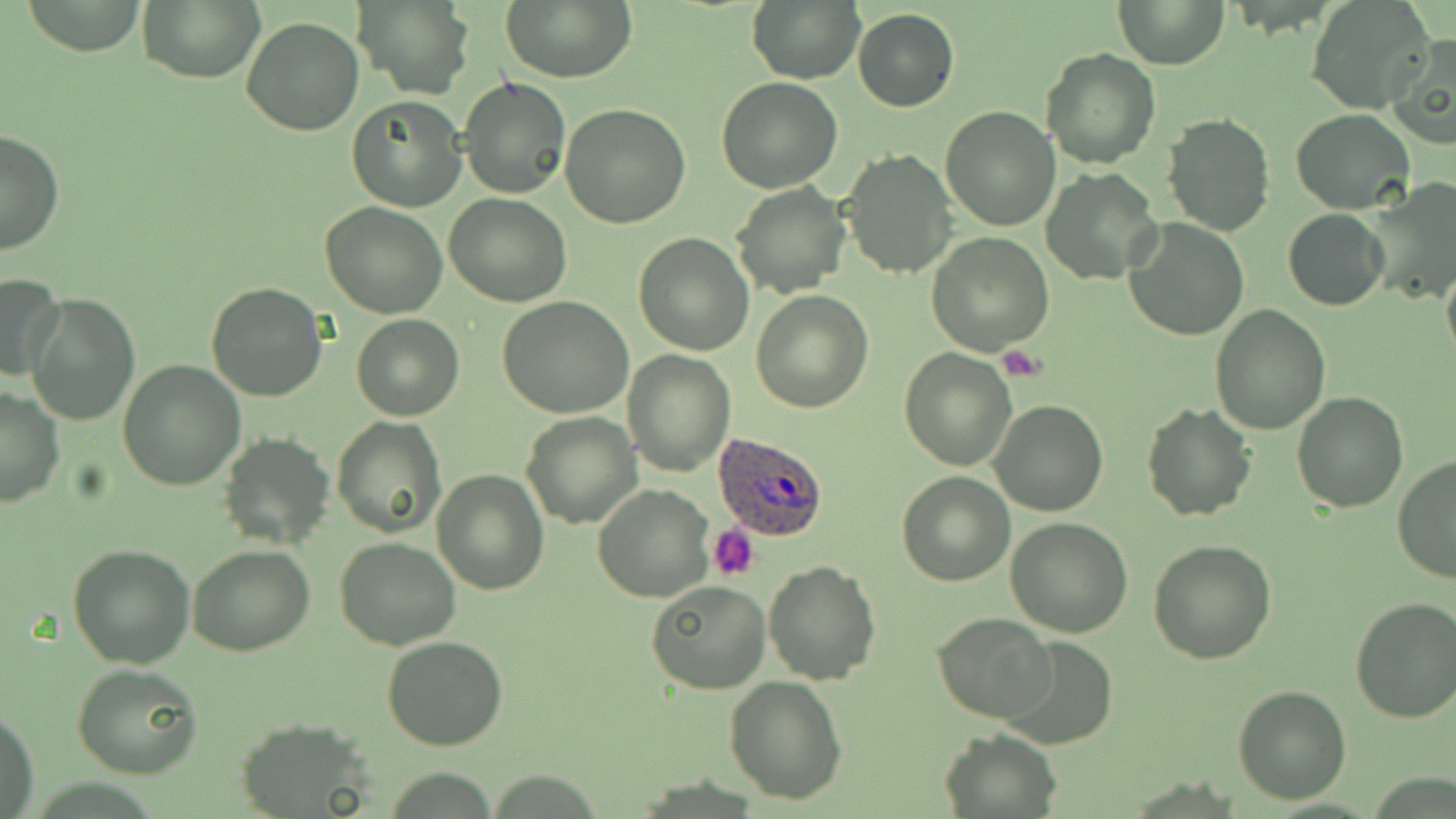 Approximate bounding boxes as (x1,y1)-(x2,y2) corner pairs in pixels. Platelet locations: (998,347)-(1048,380), (708,524)-(760,579). Plasmodium ovale-infected red blood cell locations: (712,431)-(828,543). Uninfected red blood cell locations: (18,0)-(150,55), (138,0)-(265,83), (353,0)-(475,99), (502,0)-(637,83), (749,0)-(867,86), (1115,0)-(1228,69), (1306,1)-(1435,114), (853,9)-(959,111), (241,16)-(363,135), (1384,32)-(1456,148), (1042,48)-(1159,169), (458,75)-(571,199), (716,76)-(842,192), (346,95)-(468,212), (560,104)-(692,227), (939,106)-(1061,229), (1290,108)-(1415,215), (1161,114)-(1276,235), (0,127)-(64,255), (840,149)-(958,280), (1042,168)-(1164,286), (1362,178)-(1456,298), (732,182)-(849,297), (444,192)-(571,306), (320,201)-(450,319), (1282,208)-(1388,312), (1123,218)-(1250,341), (632,231)-(756,355), (926,233)-(1053,354), (1442,262)-(1456,368), (0,272)-(65,381), (206,282)-(328,402), (751,289)-(873,411), (27,293)-(139,426), (496,295)-(634,418), (1209,304)-(1331,435), (351,314)-(463,420), (899,348)-(1017,471), (623,350)-(735,476), (117,361)-(246,490), (0,387)-(65,507), (1292,390)-(1407,511), (989,398)-(1108,518), (1141,402)-(1257,522), (521,412)-(641,528), (332,416)-(446,537), (218,432)-(335,551), (1392,455)-(1456,586), (431,469)-(549,594), (896,471)-(1014,586), (593,484)-(714,602), (1005,518)-(1134,637), (334,537)-(462,651), (1148,538)-(1276,664), (68,542)-(197,667), (188,544)-(314,657), (764,560)-(883,684), (645,580)-(770,694), (1349,597)-(1456,724), (933,613)-(1056,724), (383,635)-(508,750), (996,635)-(1119,748), (72,664)-(204,779), (724,676)-(847,804), (1232,684)-(1353,804), (1,709)-(41,819), (232,718)-(376,816), (940,728)-(1060,818). Slide-level diagnosis: Plasmodium ovale. Light microscopy. One field of a larger specimen. Captured at 1000x magnification. Image is 1456×819 pixels. May-Grünwald-Giemsa stain. Thin blood film.